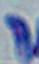

Micrograph. 1000x magnification. Toxoplasma gondii is shown.